Give the preparation type.
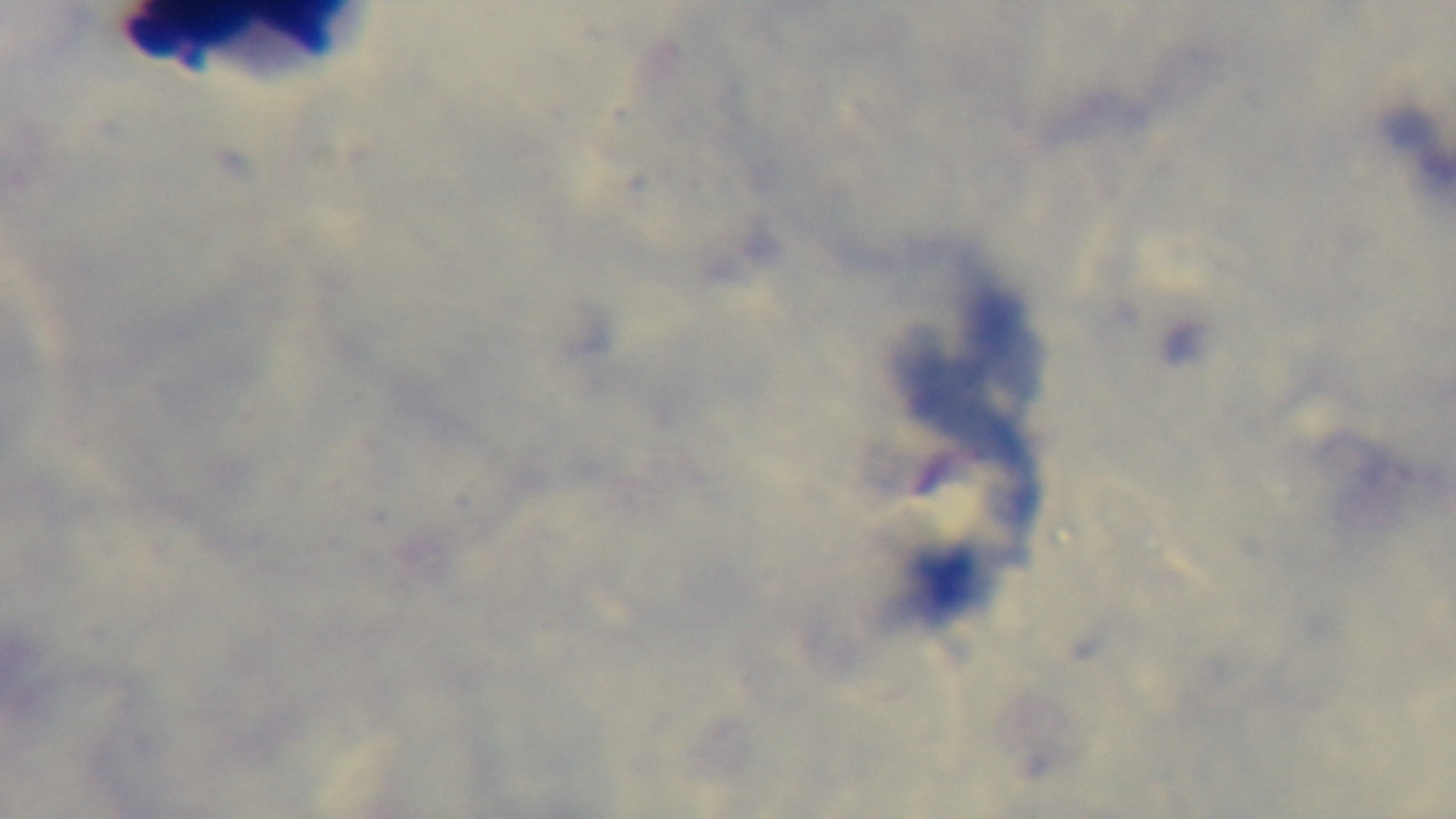

It is a thick blood film.

stain: Giemsa
capture: mounted 4K digital camera
malaria_status: uninfected
modality: light microscopy
field_of_view: single
objective: 100x oil immersion